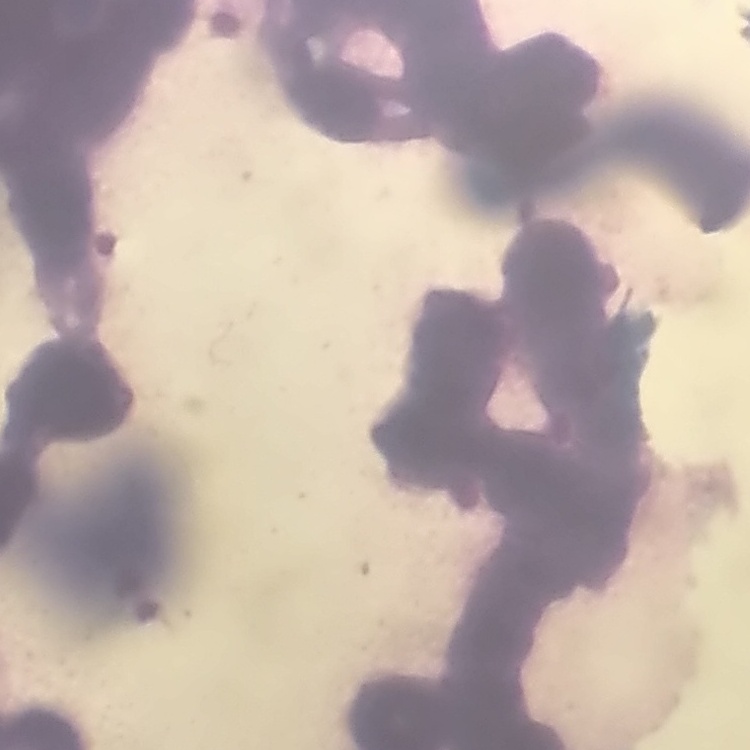
The erythrocytes exhibit rouleaux formation. Thin blood smear. Stained with either Field's or Giemsa. One tile cut from a larger photomicrograph.